Identify the blood parasite species.
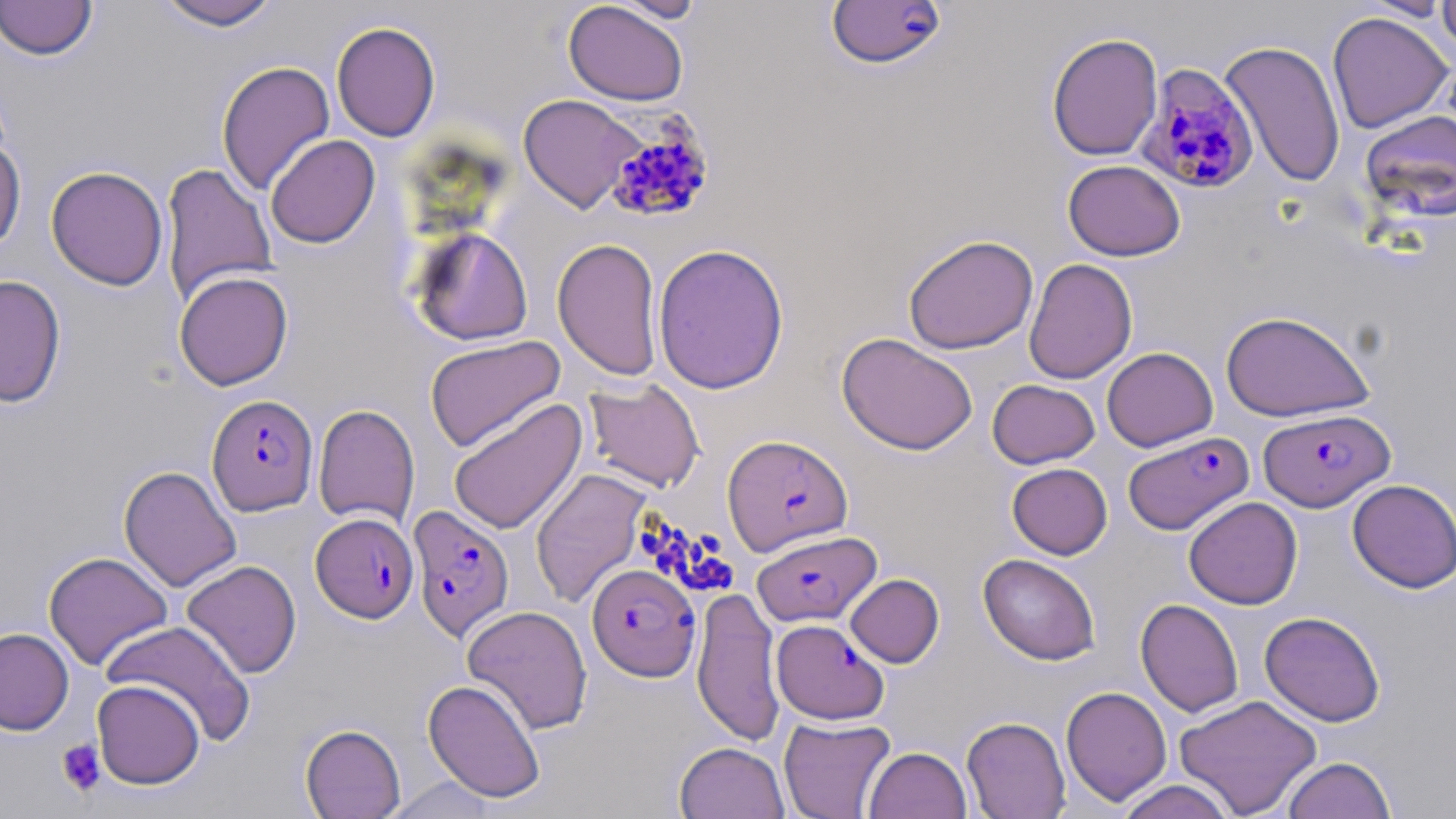
Plasmodium falciparum.

Approximate bounding boxes as (x1,y1)-(x2,y2) corner pairs in pixels. Plasmodium falciparum-infected red blood cell locations: (826,1)-(947,70), (1137,63)-(1260,194), (606,120)-(716,224), (207,394)-(318,516), (1259,408)-(1393,511), (1124,431)-(1253,535), (723,434)-(853,555), (407,505)-(514,642), (310,513)-(419,623), (752,529)-(880,626), (587,564)-(700,681), (772,619)-(888,725). Uninfected red blood cell locations: (0,0)-(98,61), (153,0)-(283,31), (610,0)-(707,23), (1359,0)-(1452,22), (1437,0)-(1456,58), (563,2)-(688,105), (1327,11)-(1454,133), (331,21)-(440,142), (1046,32)-(1163,161), (1219,40)-(1346,188), (216,61)-(335,195), (518,94)-(647,213), (1359,109)-(1456,223), (0,134)-(26,254), (265,134)-(380,249), (1062,159)-(1185,261), (161,162)-(276,305), (46,166)-(168,290), (412,228)-(533,346), (902,234)-(1039,354), (552,237)-(663,381), (652,243)-(789,394), (1023,258)-(1138,385), (174,270)-(293,390), (0,273)-(66,408), (1220,310)-(1375,422), (836,332)-(977,455), (424,335)-(565,453), (1102,347)-(1217,451), (584,378)-(705,493), (987,379)-(1100,469), (448,398)-(587,535), (313,404)-(420,528), (1007,463)-(1112,559), (118,465)-(242,592), (531,468)-(651,608), (1347,479)-(1456,594), (1183,496)-(1302,609), (43,551)-(173,670), (978,553)-(1101,665), (181,560)-(302,679), (845,574)-(944,667), (692,586)-(785,746), (1136,598)-(1244,718), (462,605)-(593,734), (1259,611)-(1386,727), (101,620)-(256,746), (0,627)-(74,734), (423,678)-(546,802), (92,680)-(205,789), (1060,686)-(1172,806), (1174,694)-(1322,818), (778,716)-(896,819), (962,716)-(1071,819), (300,723)-(405,818), (674,741)-(789,818), (864,746)-(972,819), (1283,756)-(1396,818), (384,776)-(499,818), (1115,780)-(1236,819). Platelet locations: (56,738)-(105,797). One field of a larger specimen. Image is 1456×819 pixels. Optical microscopy. Thin blood film. May-Grünwald-Giemsa-stained preparation. Captured at 1000x magnification.